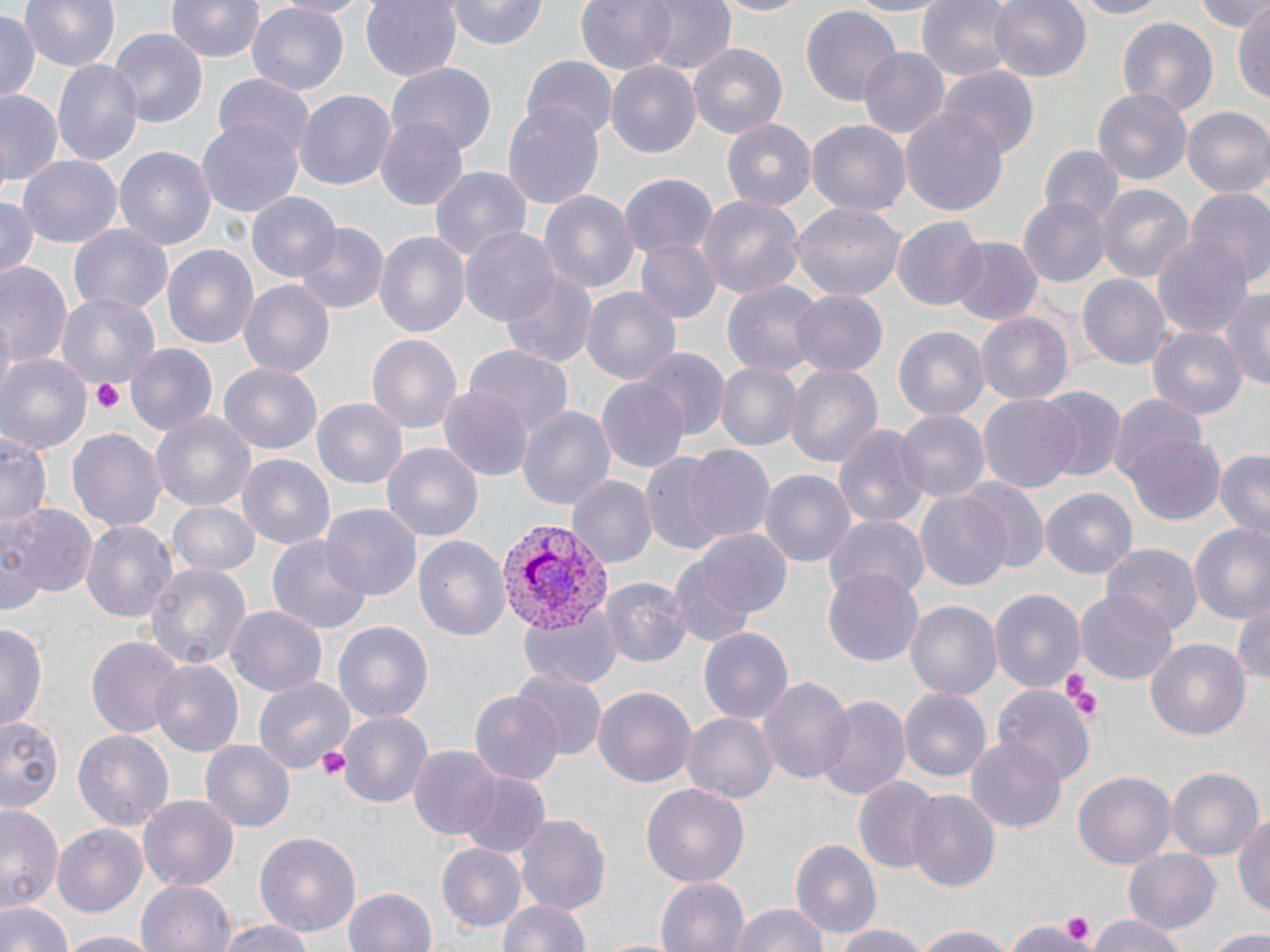
Summary:
  - Coordinate format: approximate bounding boxes as named x1/y1/x2/y2 corners in pixels
  - Platelet locations: (x1=91, y1=379, x2=125, y2=415), (x1=1064, y1=674, x2=1101, y2=719), (x1=314, y1=744, x2=350, y2=780), (x1=1056, y1=910, x2=1096, y2=944), (x1=1014, y1=917, x2=1088, y2=952)
  - Uninfected red blood cell locations: (x1=20, y1=0, x2=121, y2=70), (x1=165, y1=0, x2=264, y2=64), (x1=271, y1=0, x2=379, y2=18), (x1=359, y1=0, x2=463, y2=81), (x1=447, y1=0, x2=550, y2=49), (x1=574, y1=0, x2=682, y2=75), (x1=638, y1=0, x2=737, y2=76), (x1=708, y1=0, x2=810, y2=17), (x1=841, y1=0, x2=954, y2=16), (x1=988, y1=0, x2=1091, y2=83), (x1=1066, y1=0, x2=1172, y2=19), (x1=1194, y1=0, x2=1268, y2=35), (x1=916, y1=1, x2=1020, y2=79), (x1=247, y1=3, x2=348, y2=95), (x1=799, y1=4, x2=901, y2=106), (x1=1233, y1=8, x2=1270, y2=102), (x1=0, y1=13, x2=38, y2=100), (x1=1116, y1=15, x2=1218, y2=117), (x1=109, y1=28, x2=210, y2=127), (x1=689, y1=43, x2=787, y2=141), (x1=856, y1=48, x2=951, y2=138), (x1=520, y1=57, x2=617, y2=141), (x1=52, y1=60, x2=142, y2=166), (x1=387, y1=63, x2=497, y2=156), (x1=606, y1=64, x2=700, y2=157), (x1=939, y1=66, x2=1039, y2=159), (x1=213, y1=74, x2=315, y2=157), (x1=1093, y1=88, x2=1194, y2=184), (x1=0, y1=90, x2=61, y2=186), (x1=293, y1=90, x2=397, y2=194), (x1=503, y1=98, x2=606, y2=212), (x1=899, y1=106, x2=1010, y2=215), (x1=1183, y1=108, x2=1270, y2=198), (x1=374, y1=116, x2=468, y2=212), (x1=198, y1=117, x2=305, y2=220), (x1=805, y1=120, x2=911, y2=220), (x1=722, y1=121, x2=816, y2=213), (x1=1040, y1=145, x2=1121, y2=226), (x1=116, y1=146, x2=216, y2=254), (x1=18, y1=156, x2=121, y2=249), (x1=427, y1=166, x2=532, y2=270), (x1=615, y1=174, x2=717, y2=264), (x1=1094, y1=184, x2=1194, y2=285), (x1=1187, y1=187, x2=1270, y2=291), (x1=539, y1=190, x2=639, y2=295), (x1=248, y1=192, x2=341, y2=281), (x1=0, y1=193, x2=40, y2=277), (x1=697, y1=194, x2=806, y2=302), (x1=1020, y1=198, x2=1108, y2=285), (x1=790, y1=201, x2=906, y2=305), (x1=893, y1=220, x2=986, y2=309), (x1=291, y1=221, x2=389, y2=315), (x1=69, y1=223, x2=173, y2=316), (x1=460, y1=226, x2=561, y2=326), (x1=374, y1=230, x2=469, y2=342), (x1=1151, y1=231, x2=1251, y2=336), (x1=633, y1=237, x2=721, y2=326), (x1=948, y1=237, x2=1043, y2=326), (x1=162, y1=243, x2=259, y2=354), (x1=0, y1=257, x2=73, y2=373), (x1=500, y1=270, x2=596, y2=368), (x1=1076, y1=271, x2=1172, y2=373), (x1=239, y1=281, x2=337, y2=378), (x1=721, y1=281, x2=822, y2=376), (x1=580, y1=287, x2=680, y2=386), (x1=1220, y1=290, x2=1270, y2=393), (x1=790, y1=291, x2=888, y2=376), (x1=56, y1=292, x2=162, y2=394), (x1=976, y1=312, x2=1072, y2=406), (x1=894, y1=324, x2=989, y2=421), (x1=1148, y1=327, x2=1246, y2=420), (x1=366, y1=332, x2=464, y2=435), (x1=126, y1=345, x2=217, y2=435), (x1=463, y1=346, x2=572, y2=443), (x1=639, y1=350, x2=729, y2=440), (x1=0, y1=354, x2=92, y2=457), (x1=714, y1=362, x2=800, y2=452), (x1=219, y1=363, x2=324, y2=453), (x1=785, y1=365, x2=883, y2=468), (x1=596, y1=376, x2=689, y2=474), (x1=438, y1=385, x2=530, y2=481), (x1=1039, y1=386, x2=1126, y2=481), (x1=1106, y1=395, x2=1207, y2=487), (x1=978, y1=396, x2=1082, y2=493), (x1=311, y1=397, x2=407, y2=488), (x1=517, y1=403, x2=615, y2=516), (x1=896, y1=410, x2=989, y2=504), (x1=152, y1=412, x2=256, y2=512), (x1=834, y1=422, x2=929, y2=530), (x1=68, y1=425, x2=167, y2=534), (x1=0, y1=432, x2=51, y2=532), (x1=1125, y1=434, x2=1224, y2=524), (x1=382, y1=444, x2=482, y2=541), (x1=681, y1=444, x2=776, y2=543), (x1=1211, y1=449, x2=1270, y2=539), (x1=236, y1=453, x2=338, y2=551), (x1=641, y1=454, x2=733, y2=553), (x1=760, y1=469, x2=854, y2=570), (x1=567, y1=476, x2=656, y2=568), (x1=963, y1=481, x2=1049, y2=574), (x1=1041, y1=487, x2=1137, y2=578), (x1=915, y1=490, x2=1011, y2=590), (x1=167, y1=500, x2=261, y2=574), (x1=7, y1=505, x2=98, y2=600), (x1=319, y1=505, x2=420, y2=602), (x1=823, y1=514, x2=929, y2=604), (x1=1187, y1=519, x2=1270, y2=622), (x1=81, y1=520, x2=178, y2=624), (x1=3, y1=529, x2=46, y2=619), (x1=683, y1=530, x2=791, y2=623), (x1=268, y1=533, x2=374, y2=637), (x1=415, y1=537, x2=511, y2=641), (x1=1100, y1=544, x2=1202, y2=636), (x1=145, y1=563, x2=250, y2=675), (x1=670, y1=566, x2=756, y2=650), (x1=822, y1=569, x2=922, y2=665), (x1=601, y1=578, x2=690, y2=668), (x1=991, y1=588, x2=1085, y2=695), (x1=1075, y1=593, x2=1176, y2=683), (x1=1231, y1=595, x2=1270, y2=688), (x1=906, y1=599, x2=1001, y2=698), (x1=517, y1=603, x2=623, y2=690), (x1=225, y1=604, x2=327, y2=696), (x1=332, y1=619, x2=435, y2=722), (x1=1, y1=623, x2=46, y2=734), (x1=701, y1=627, x2=793, y2=724), (x1=86, y1=635, x2=185, y2=739), (x1=1146, y1=639, x2=1251, y2=739), (x1=151, y1=660, x2=244, y2=757), (x1=513, y1=669, x2=606, y2=760), (x1=759, y1=674, x2=853, y2=785), (x1=253, y1=675, x2=355, y2=773), (x1=593, y1=685, x2=696, y2=790), (x1=993, y1=686, x2=1094, y2=785), (x1=899, y1=689, x2=990, y2=783), (x1=469, y1=692, x2=563, y2=786), (x1=816, y1=695, x2=910, y2=803), (x1=338, y1=710, x2=433, y2=808), (x1=682, y1=712, x2=778, y2=803), (x1=0, y1=717, x2=63, y2=808), (x1=73, y1=729, x2=175, y2=832), (x1=965, y1=733, x2=1068, y2=832), (x1=199, y1=740, x2=293, y2=832), (x1=408, y1=744, x2=502, y2=841), (x1=1166, y1=767, x2=1261, y2=862), (x1=456, y1=770, x2=551, y2=858), (x1=1073, y1=770, x2=1176, y2=871), (x1=853, y1=776, x2=942, y2=874), (x1=640, y1=783, x2=750, y2=890), (x1=906, y1=790, x2=1001, y2=891), (x1=138, y1=794, x2=240, y2=891), (x1=0, y1=804, x2=64, y2=914), (x1=1234, y1=809, x2=1270, y2=922), (x1=515, y1=814, x2=610, y2=912), (x1=53, y1=823, x2=149, y2=919), (x1=253, y1=829, x2=362, y2=937), (x1=789, y1=837, x2=881, y2=937), (x1=437, y1=842, x2=526, y2=931), (x1=1119, y1=848, x2=1220, y2=935), (x1=655, y1=877, x2=749, y2=952), (x1=137, y1=879, x2=235, y2=952), (x1=343, y1=888, x2=437, y2=952), (x1=497, y1=896, x2=593, y2=952), (x1=0, y1=898, x2=73, y2=952), (x1=729, y1=903, x2=829, y2=952), (x1=1085, y1=914, x2=1190, y2=952), (x1=213, y1=918, x2=321, y2=952), (x1=1006, y1=919, x2=1088, y2=951), (x1=910, y1=924, x2=1018, y2=952), (x1=831, y1=926, x2=931, y2=952), (x1=1202, y1=929, x2=1270, y2=950), (x1=56, y1=931, x2=157, y2=952)
  - Plasmodium vivax-infected red blood cell locations: (x1=492, y1=517, x2=614, y2=628)
  - Slide-level diagnosis: Plasmodium vivax
  - Magnification: 1000x
  - Modality: light microscopy
  - Image size: 1270×952 pixels
  - Preparation: thin blood smear
  - Field of view: single
  - Stain: May-Grünwald-Giemsa